Give the extent of all Plasmodium vivax-infected red blood cells.
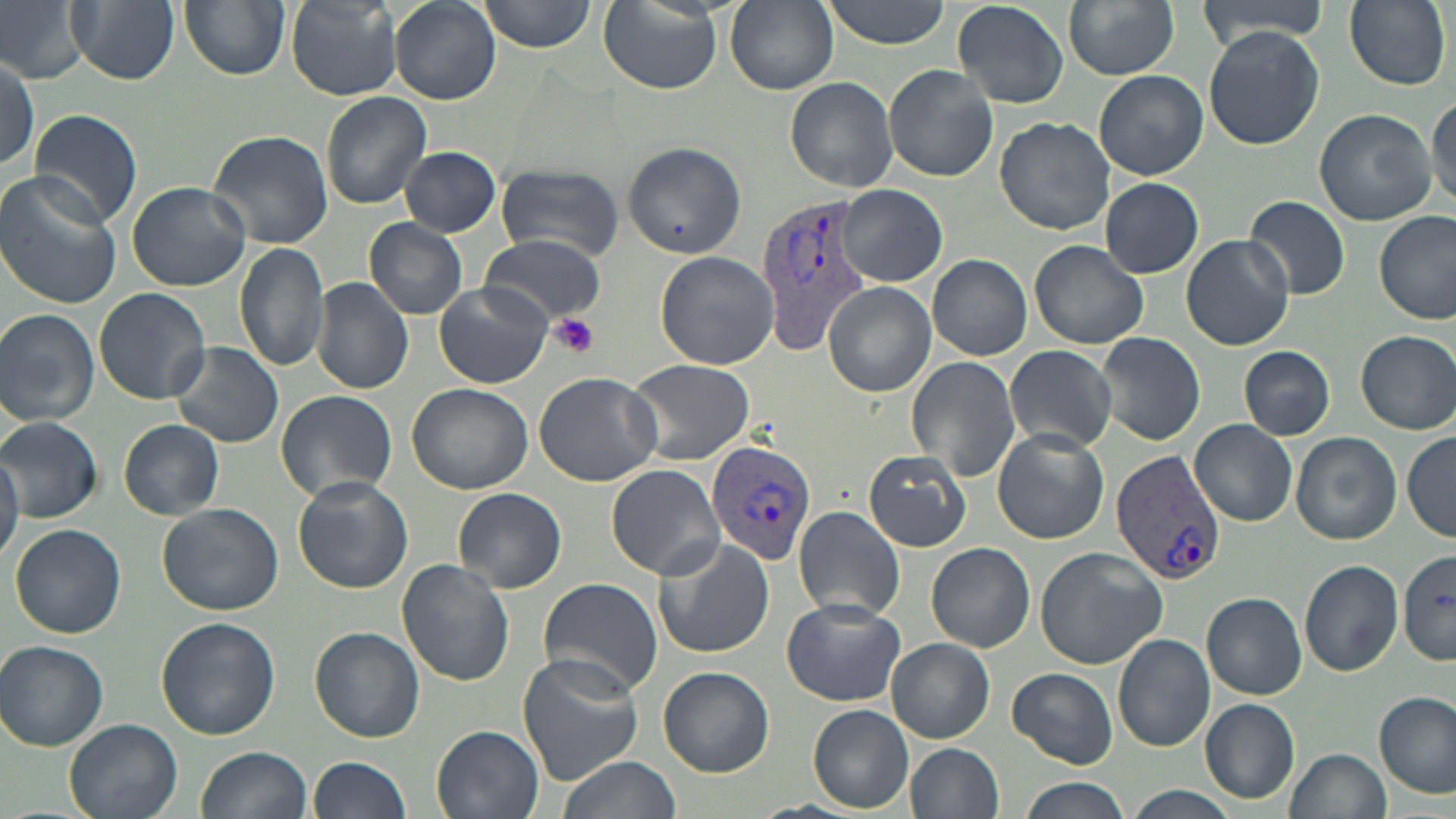
Approximate bounding boxes as named x1/y1/x2/y2 corners in pixels.
Plasmodium vivax-infected red blood cells: (x1=755, y1=194, x2=873, y2=352), (x1=706, y1=441, x2=819, y2=568), (x1=1110, y1=448, x2=1225, y2=586).

Summary:
  - Uninfected red blood cell locations: (x1=1, y1=0, x2=93, y2=84), (x1=68, y1=0, x2=178, y2=85), (x1=180, y1=0, x2=290, y2=80), (x1=480, y1=0, x2=595, y2=52), (x1=822, y1=0, x2=952, y2=48), (x1=1064, y1=0, x2=1180, y2=79), (x1=1201, y1=0, x2=1329, y2=50), (x1=1343, y1=0, x2=1450, y2=91), (x1=285, y1=1, x2=402, y2=100), (x1=388, y1=1, x2=499, y2=104), (x1=726, y1=1, x2=838, y2=94), (x1=952, y1=1, x2=1070, y2=109), (x1=599, y1=4, x2=724, y2=94), (x1=1203, y1=25, x2=1324, y2=151), (x1=1, y1=52, x2=38, y2=175), (x1=883, y1=63, x2=997, y2=181), (x1=1095, y1=70, x2=1208, y2=180), (x1=784, y1=77, x2=900, y2=192), (x1=320, y1=92, x2=432, y2=209), (x1=1428, y1=92, x2=1456, y2=208), (x1=27, y1=108, x2=144, y2=225), (x1=1314, y1=108, x2=1437, y2=225), (x1=996, y1=116, x2=1115, y2=236), (x1=207, y1=130, x2=332, y2=249), (x1=620, y1=141, x2=746, y2=258), (x1=400, y1=146, x2=501, y2=236), (x1=495, y1=163, x2=623, y2=261), (x1=0, y1=171, x2=121, y2=311), (x1=1099, y1=178, x2=1203, y2=278), (x1=126, y1=181, x2=250, y2=292), (x1=838, y1=184, x2=947, y2=287), (x1=1245, y1=196, x2=1350, y2=299), (x1=1375, y1=209, x2=1456, y2=325), (x1=365, y1=218, x2=467, y2=319), (x1=481, y1=234, x2=608, y2=324), (x1=1181, y1=234, x2=1294, y2=351), (x1=1028, y1=239, x2=1149, y2=350), (x1=235, y1=242, x2=330, y2=372), (x1=656, y1=251, x2=778, y2=369), (x1=927, y1=254, x2=1032, y2=360), (x1=311, y1=277, x2=413, y2=396), (x1=824, y1=282, x2=936, y2=397), (x1=435, y1=284, x2=552, y2=388), (x1=92, y1=287, x2=211, y2=405), (x1=0, y1=308, x2=101, y2=426), (x1=128, y1=316, x2=275, y2=424), (x1=1356, y1=329, x2=1456, y2=434), (x1=1095, y1=331, x2=1205, y2=445), (x1=170, y1=342, x2=284, y2=450), (x1=1004, y1=344, x2=1117, y2=454), (x1=1239, y1=346, x2=1335, y2=440), (x1=905, y1=355, x2=1019, y2=484), (x1=624, y1=357, x2=757, y2=467), (x1=533, y1=372, x2=662, y2=486), (x1=406, y1=384, x2=532, y2=494), (x1=273, y1=390, x2=398, y2=502), (x1=1, y1=416, x2=101, y2=522), (x1=119, y1=419, x2=222, y2=519), (x1=1191, y1=419, x2=1298, y2=527), (x1=992, y1=428, x2=1109, y2=544), (x1=1291, y1=431, x2=1402, y2=546), (x1=1402, y1=432, x2=1456, y2=542), (x1=865, y1=450, x2=973, y2=551), (x1=0, y1=451, x2=22, y2=565), (x1=607, y1=464, x2=726, y2=580), (x1=292, y1=477, x2=412, y2=594), (x1=454, y1=487, x2=566, y2=595), (x1=157, y1=503, x2=283, y2=616), (x1=792, y1=505, x2=907, y2=622), (x1=10, y1=523, x2=127, y2=639), (x1=653, y1=536, x2=775, y2=660), (x1=927, y1=543, x2=1036, y2=653), (x1=1034, y1=546, x2=1169, y2=669), (x1=1397, y1=549, x2=1456, y2=664), (x1=398, y1=560, x2=516, y2=686), (x1=1298, y1=560, x2=1405, y2=677), (x1=536, y1=578, x2=663, y2=698), (x1=1202, y1=592, x2=1306, y2=699), (x1=782, y1=598, x2=906, y2=706), (x1=156, y1=616, x2=280, y2=739), (x1=310, y1=628, x2=424, y2=742), (x1=1113, y1=634, x2=1216, y2=752), (x1=888, y1=638, x2=994, y2=743), (x1=1, y1=640, x2=109, y2=750), (x1=518, y1=654, x2=643, y2=783), (x1=659, y1=667, x2=774, y2=777), (x1=1007, y1=668, x2=1119, y2=767), (x1=1375, y1=691, x2=1454, y2=798), (x1=1199, y1=698, x2=1299, y2=802), (x1=808, y1=704, x2=914, y2=813), (x1=64, y1=718, x2=184, y2=819), (x1=431, y1=725, x2=544, y2=819), (x1=905, y1=743, x2=1004, y2=819), (x1=196, y1=746, x2=311, y2=819), (x1=1284, y1=748, x2=1390, y2=819), (x1=310, y1=756, x2=411, y2=819), (x1=554, y1=757, x2=682, y2=819), (x1=1019, y1=777, x2=1130, y2=819), (x1=1129, y1=785, x2=1240, y2=819)
  - Platelet locations: (x1=550, y1=315, x2=601, y2=358)
  - Slide-level diagnosis: Plasmodium vivax
  - Field of view: one of a larger specimen
  - Image size: 1456×819 pixels
  - Modality: light microscopy
  - Magnification: 1000x
  - Stain: May-Grünwald-Giemsa
  - Preparation: thin blood film